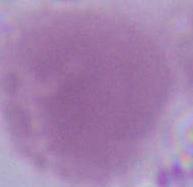

identification: red blood cell
modality: micrograph
magnification: 1000x